Classify this cell by malaria status.
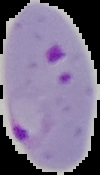

It is parasitized.

image_type: segmented cell region with the area outside set to black
image_size: 100×175 pixels
preparation: thin blood film